Classify this cell by malaria status.
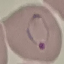
It is parasitized.

Summary:
  - Preparation: thin blood film
  - Image type: cell patch, automatically extracted from a larger field of view and resized to 64 × 64 pixels
  - Capture: smartphone camera at the microscope eyepiece
  - Stain: Giemsa